Assess this cell for malaria.
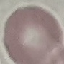

It is uninfected.

Thin blood smear. Automatically extracted cell patch, resized to 64 × 64 pixels. Acquired by smartphone through the microscope eyepiece. Giemsa stain.